Comment on the morphology of the erythrocytes.
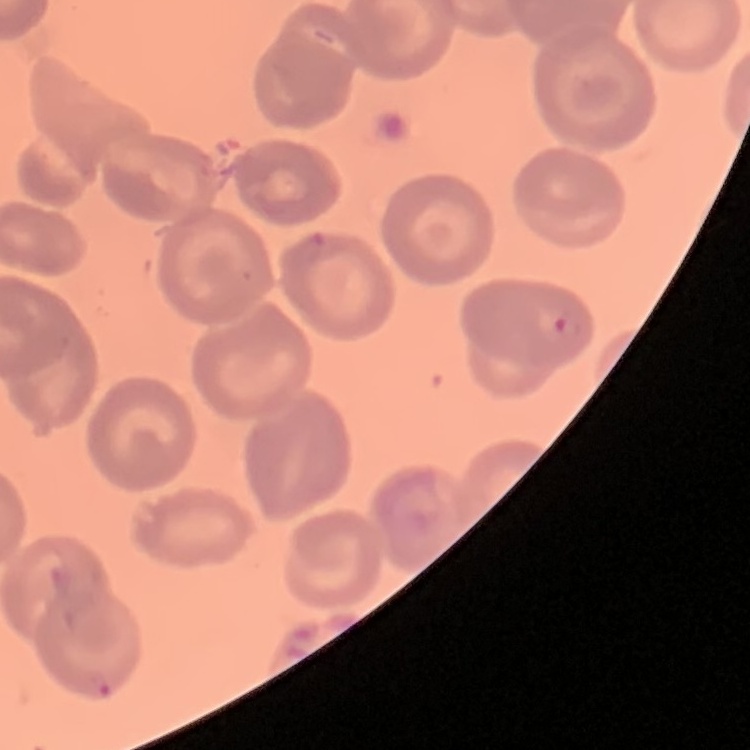
No rouleaux formation.

Summary:
  - Preparation: thin peripheral smear
  - Stain: Field's or Giemsa
  - Image type: square crop of a larger photomicrograph